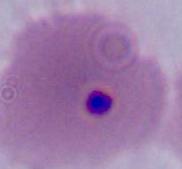

magnification: 400x or 1000x
modality: photomicrograph
identification: Plasmodium